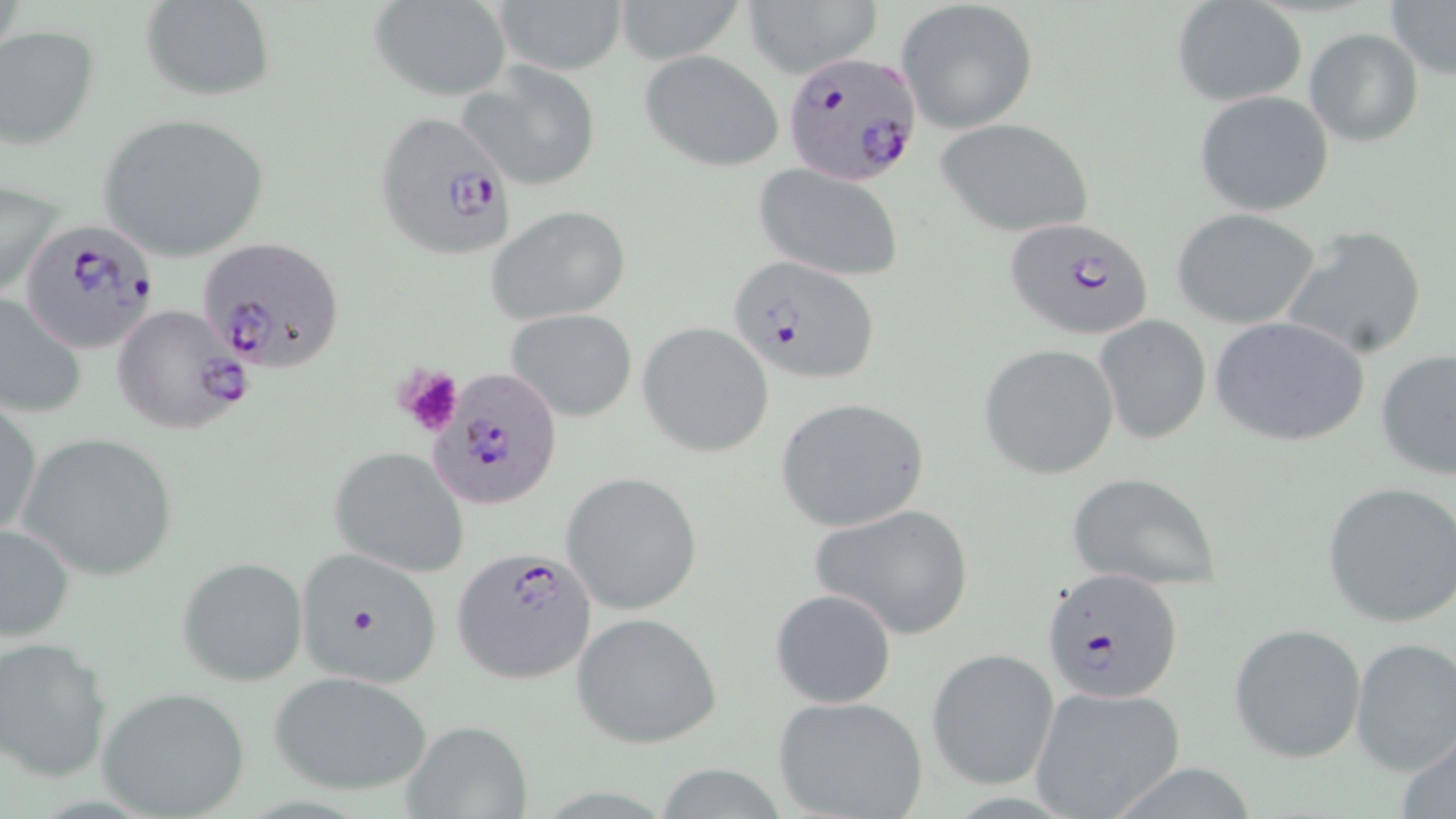
Summary:
  - Coordinate format: approximate bounding boxes as named x1/y1/x2/y2 corners in pixels
  - Platelet locations: (x1=395, y1=365, x2=462, y2=436)
  - Plasmodium falciparum-infected red blood cell locations: (x1=783, y1=53, x2=922, y2=202), (x1=373, y1=109, x2=520, y2=262), (x1=1004, y1=217, x2=1155, y2=343), (x1=18, y1=220, x2=161, y2=354), (x1=200, y1=237, x2=345, y2=374), (x1=726, y1=254, x2=879, y2=385), (x1=109, y1=303, x2=253, y2=436), (x1=428, y1=369, x2=566, y2=511), (x1=451, y1=545, x2=598, y2=684), (x1=1041, y1=568, x2=1184, y2=703)
  - Uninfected red blood cell locations: (x1=140, y1=0, x2=275, y2=100), (x1=492, y1=0, x2=630, y2=75), (x1=609, y1=0, x2=750, y2=64), (x1=1384, y1=0, x2=1455, y2=81), (x1=369, y1=1, x2=512, y2=102), (x1=745, y1=1, x2=882, y2=79), (x1=897, y1=1, x2=1039, y2=134), (x1=1172, y1=1, x2=1308, y2=106), (x1=0, y1=26, x2=100, y2=150), (x1=1304, y1=27, x2=1425, y2=147), (x1=640, y1=50, x2=785, y2=173), (x1=458, y1=61, x2=603, y2=192), (x1=1194, y1=89, x2=1334, y2=216), (x1=97, y1=112, x2=271, y2=262), (x1=933, y1=116, x2=1095, y2=238), (x1=753, y1=165, x2=904, y2=281), (x1=1, y1=177, x2=63, y2=305), (x1=486, y1=204, x2=632, y2=324), (x1=1172, y1=207, x2=1322, y2=329), (x1=1280, y1=225, x2=1429, y2=360), (x1=0, y1=290, x2=88, y2=418), (x1=505, y1=308, x2=638, y2=422), (x1=1209, y1=315, x2=1370, y2=448), (x1=1096, y1=316, x2=1212, y2=445), (x1=636, y1=322, x2=773, y2=457), (x1=978, y1=344, x2=1120, y2=479), (x1=1375, y1=348, x2=1455, y2=482), (x1=774, y1=397, x2=927, y2=531), (x1=0, y1=402, x2=43, y2=539), (x1=18, y1=434, x2=181, y2=583), (x1=328, y1=447, x2=472, y2=577), (x1=1067, y1=470, x2=1224, y2=592), (x1=560, y1=471, x2=704, y2=616), (x1=1321, y1=482, x2=1456, y2=629), (x1=810, y1=502, x2=975, y2=640), (x1=0, y1=523, x2=75, y2=642), (x1=292, y1=547, x2=448, y2=691), (x1=177, y1=556, x2=308, y2=686), (x1=770, y1=588, x2=897, y2=709), (x1=571, y1=612, x2=723, y2=749), (x1=1229, y1=622, x2=1367, y2=763), (x1=0, y1=636, x2=115, y2=783), (x1=1350, y1=637, x2=1456, y2=777), (x1=925, y1=648, x2=1058, y2=789), (x1=267, y1=670, x2=434, y2=799), (x1=96, y1=686, x2=252, y2=818), (x1=1029, y1=686, x2=1187, y2=819), (x1=774, y1=695, x2=929, y2=819), (x1=399, y1=722, x2=532, y2=817), (x1=1395, y1=728, x2=1456, y2=819)
  - Slide-level diagnosis: Plasmodium falciparum
  - Stain: May-Grünwald-Giemsa
  - Modality: optical microscopy
  - Field of view: one of a larger specimen
  - Magnification: 1000x
  - Image size: 1456×819 pixels
  - Preparation: thin blood film